Name the blood parasite species.
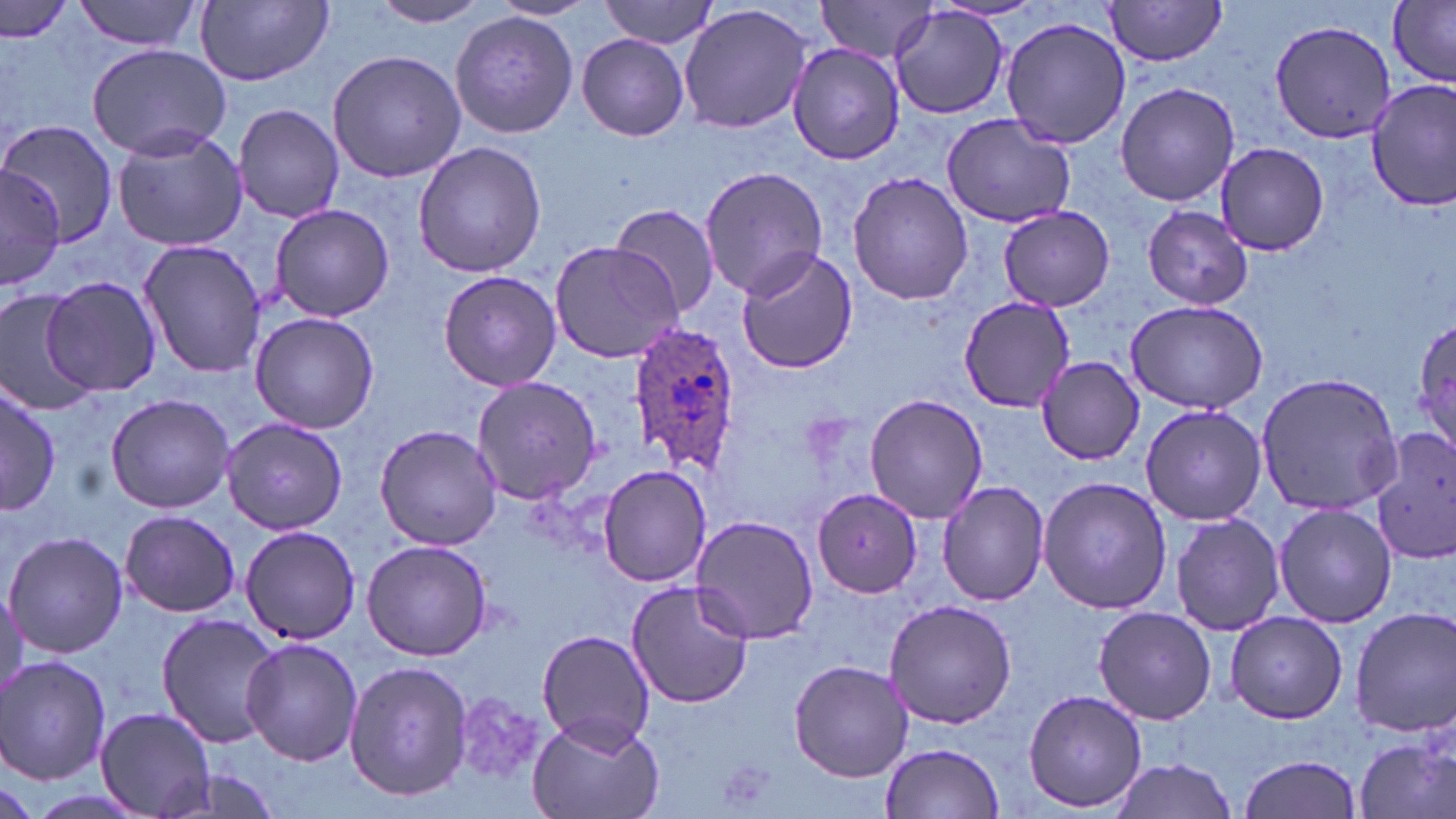

Plasmodium ovale.

image_size: 1456×819 pixels
plasmodium_ovale_infected_red_blood_cell_locations: 'approximate bounding boxes as (x1,y1)-(x2,y2) corner pairs in pixels: (626,320)-(744,474)'
uninfected_red_blood_cell_locations: 'approximate bounding boxes as (x1,y1)-(x2,y2) corner pairs in pixels: (74,0)-(204,53), (195,1)-(334,85), (371,1)-(493,26), (491,1)-(599,21), (597,1)-(719,49), (819,1)-(943,63), (1103,1)-(1230,66), (0,2)-(75,44), (1388,2)-(1454,86), (678,4)-(812,135), (890,6)-(1011,120), (449,11)-(578,138), (1000,17)-(1131,150), (1270,19)-(1393,144), (575,33)-(690,140), (788,42)-(906,166), (87,44)-(231,160), (326,49)-(466,183), (1365,77)-(1456,210), (1115,81)-(1240,207), (233,102)-(343,224), (941,112)-(1076,228), (0,120)-(122,251), (112,127)-(248,253), (411,140)-(548,278), (1215,142)-(1330,255), (699,165)-(828,299), (0,166)-(66,286), (847,170)-(973,306), (608,204)-(721,320), (269,205)-(396,321), (997,206)-(1115,312), (1143,206)-(1251,309), (137,239)-(268,379), (547,239)-(684,364), (734,247)-(859,374), (437,268)-(561,391), (42,277)-(161,397), (0,289)-(95,415), (958,295)-(1074,413), (1123,299)-(1269,416), (249,312)-(379,433), (1410,313)-(1456,459), (1035,355)-(1147,464), (1254,373)-(1403,515), (471,376)-(602,503), (0,377)-(58,518), (862,393)-(988,522), (105,394)-(233,512), (1140,403)-(1267,526), (223,419)-(348,533), (374,423)-(503,549), (1368,428)-(1456,562), (597,464)-(712,587), (1035,475)-(1173,614), (938,481)-(1050,605), (812,487)-(925,598), (1274,502)-(1397,628), (119,509)-(242,618), (1169,511)-(1284,637), (691,514)-(818,646), (240,524)-(362,645), (4,532)-(129,659), (362,539)-(492,661), (625,580)-(754,709), (884,599)-(1017,729), (1093,606)-(1216,724), (1349,607)-(1456,737), (1225,612)-(1349,724), (156,614)-(286,748), (535,630)-(656,752), (241,638)-(363,766), (1,656)-(112,785), (344,660)-(474,800), (788,660)-(914,781), (1019,688)-(1147,813), (447,690)-(548,786), (97,706)-(218,818), (526,714)-(664,819), (1353,733)-(1454,819), (881,743)-(1004,818), (1237,753)-(1363,819), (1109,759)-(1241,816), (157,766)-(293,818)'
stain: May-Grünwald-Giemsa
preparation: thin blood smear
field_of_view: single
modality: optical microscopy
magnification: 1000x